Outline each uninfected red blood cell.
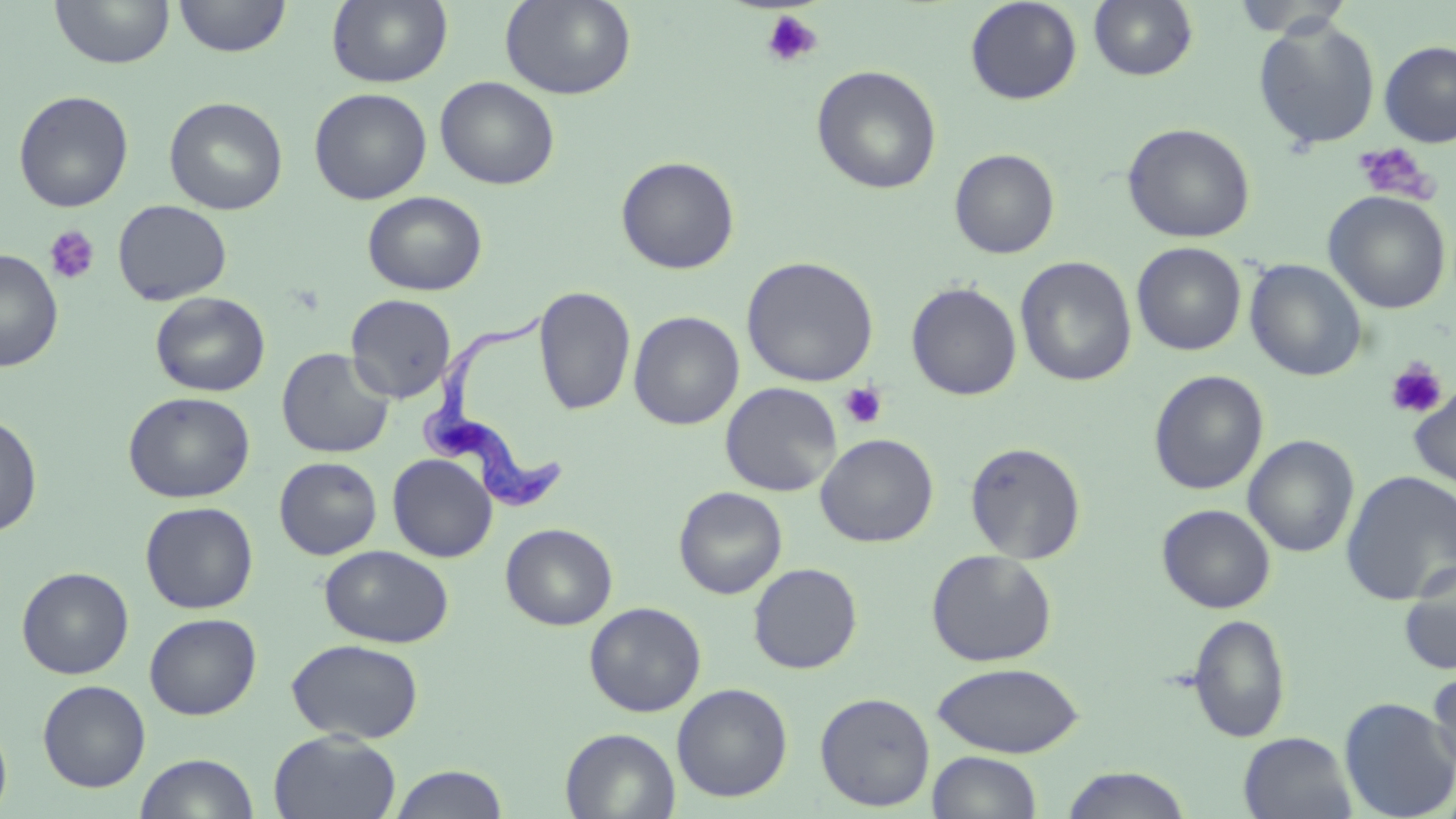

Approximate bounding boxes as named x1/y1/x2/y2 corners in pixels.
Uninfected red blood cells: (x1=49, y1=0, x2=175, y2=69), (x1=174, y1=0, x2=291, y2=58), (x1=327, y1=0, x2=453, y2=88), (x1=501, y1=0, x2=636, y2=100), (x1=964, y1=0, x2=1083, y2=105), (x1=1088, y1=0, x2=1198, y2=82), (x1=1230, y1=1, x2=1354, y2=39), (x1=1253, y1=17, x2=1381, y2=150), (x1=1378, y1=40, x2=1456, y2=148), (x1=811, y1=65, x2=942, y2=195), (x1=435, y1=76, x2=560, y2=190), (x1=308, y1=87, x2=432, y2=205), (x1=13, y1=90, x2=134, y2=213), (x1=164, y1=96, x2=288, y2=215), (x1=1122, y1=122, x2=1256, y2=243), (x1=949, y1=149, x2=1060, y2=259), (x1=615, y1=156, x2=740, y2=274), (x1=1323, y1=190, x2=1452, y2=314), (x1=362, y1=191, x2=488, y2=295), (x1=113, y1=199, x2=232, y2=305), (x1=1131, y1=242, x2=1246, y2=356), (x1=0, y1=248, x2=63, y2=372), (x1=741, y1=255, x2=879, y2=387), (x1=1015, y1=256, x2=1137, y2=387), (x1=1245, y1=259, x2=1368, y2=382), (x1=905, y1=281, x2=1022, y2=401), (x1=533, y1=285, x2=636, y2=416), (x1=150, y1=291, x2=271, y2=397), (x1=345, y1=294, x2=456, y2=403), (x1=628, y1=311, x2=744, y2=431), (x1=276, y1=347, x2=394, y2=459), (x1=1148, y1=369, x2=1269, y2=495), (x1=720, y1=382, x2=842, y2=497), (x1=1408, y1=382, x2=1456, y2=495), (x1=123, y1=391, x2=255, y2=503), (x1=0, y1=412, x2=42, y2=538), (x1=816, y1=433, x2=939, y2=547), (x1=1243, y1=434, x2=1359, y2=558), (x1=965, y1=441, x2=1086, y2=563), (x1=387, y1=454, x2=497, y2=562), (x1=274, y1=456, x2=382, y2=560), (x1=1340, y1=469, x2=1455, y2=605), (x1=674, y1=486, x2=788, y2=599), (x1=140, y1=501, x2=259, y2=614), (x1=1157, y1=504, x2=1276, y2=613), (x1=500, y1=523, x2=618, y2=630), (x1=320, y1=545, x2=453, y2=648), (x1=926, y1=549, x2=1057, y2=667), (x1=1398, y1=560, x2=1456, y2=675), (x1=748, y1=563, x2=863, y2=674), (x1=16, y1=566, x2=134, y2=679), (x1=584, y1=601, x2=706, y2=717), (x1=144, y1=613, x2=262, y2=720), (x1=1188, y1=613, x2=1291, y2=743), (x1=286, y1=638, x2=424, y2=743), (x1=930, y1=661, x2=1085, y2=758), (x1=1426, y1=669, x2=1456, y2=779), (x1=37, y1=679, x2=151, y2=792), (x1=672, y1=683, x2=793, y2=802), (x1=815, y1=691, x2=936, y2=811), (x1=1338, y1=697, x2=1456, y2=818), (x1=0, y1=715, x2=12, y2=818), (x1=561, y1=728, x2=679, y2=819), (x1=269, y1=730, x2=401, y2=818), (x1=1238, y1=732, x2=1358, y2=819), (x1=927, y1=750, x2=1043, y2=818), (x1=134, y1=752, x2=260, y2=818), (x1=389, y1=764, x2=508, y2=819), (x1=1059, y1=767, x2=1192, y2=818).

Trypanosoma brucei locations: (x1=415, y1=310, x2=569, y2=516). Platelet locations: (x1=761, y1=11, x2=823, y2=68), (x1=1353, y1=143, x2=1437, y2=205), (x1=44, y1=225, x2=101, y2=285), (x1=1384, y1=358, x2=1448, y2=420), (x1=839, y1=382, x2=888, y2=429). Slide-level diagnosis: Trypanosoma brucei. Captured at 1000x magnification. Light microscopy. Image is 1456×819 pixels. May-Grünwald-Giemsa-stained preparation. Thin blood smear. Single field of view.